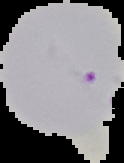
malaria status = parasitized
image size = 124×163 pixels
image type = segmented cell region with the area outside set to black
preparation = thin blood smear